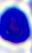

Summary:
  - Identification: white blood cell
  - Magnification: 400x
  - Modality: photomicrograph